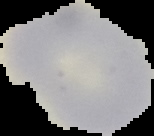
{
  "image_size": "154×136 pixels",
  "image_type": "cell region segmented out of the field of view; surrounding area masked to black",
  "result": "no Plasmodium parasites seen",
  "preparation": "thin blood film"
}